Report the malaria status of this cell.
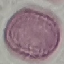
Uninfected.

Summary:
  - Capture: smartphone through the microscope eyepiece
  - Stain: Giemsa
  - Preparation: thin blood film
  - Image type: cell patch, automatically extracted from a larger field of view and resized to 64 × 64 pixels